Name the blood parasite species.
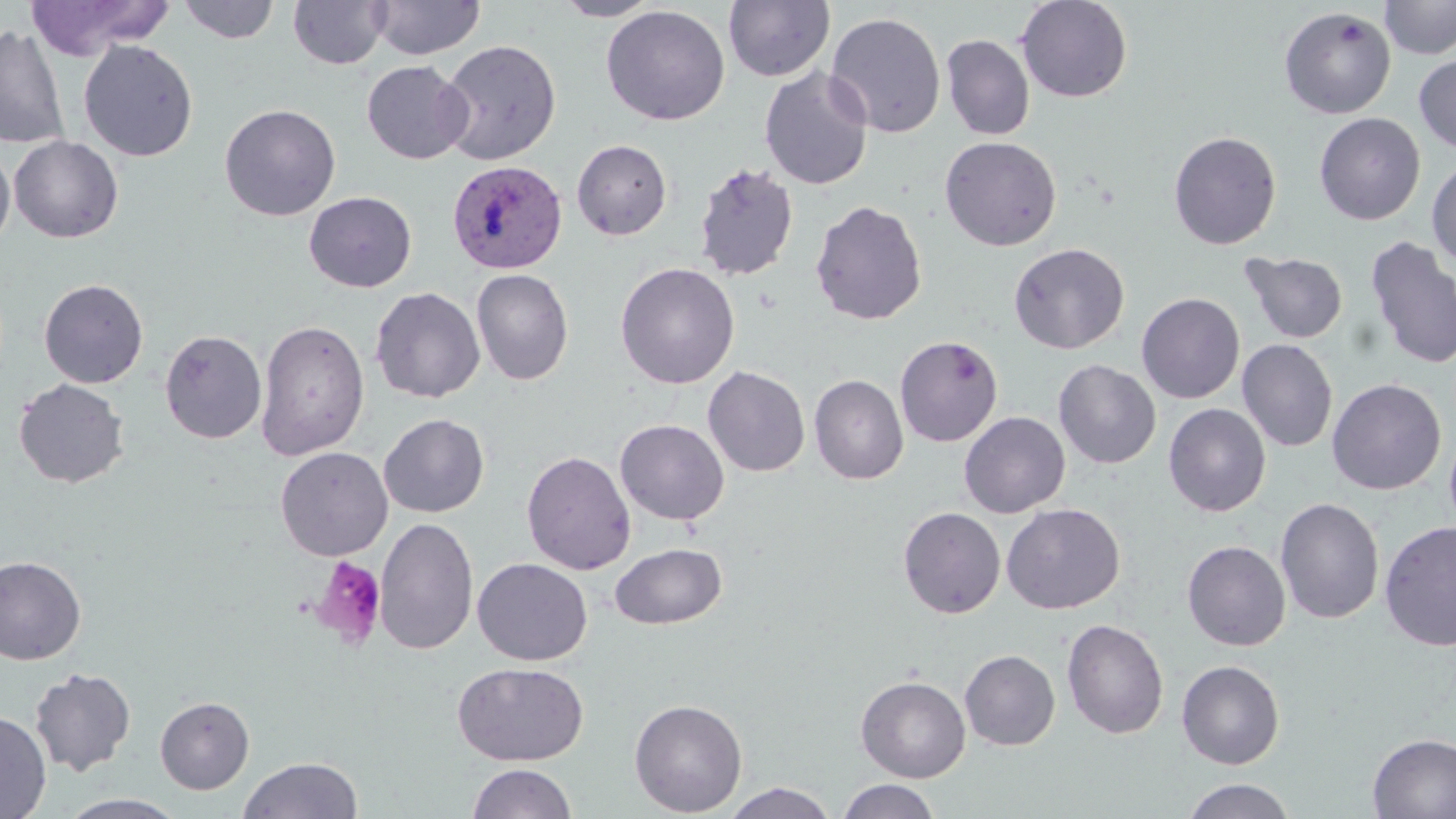
Plasmodium vivax.

{
  "platelet_locations": "approximate bounding boxes as (x1, y1, x2, y2) in pixels: (310, 555, 387, 649)",
  "plasmodium_vivax_infected_red_blood_cell_locations": "approximate bounding boxes as (x1, y1, x2, y2) in pixels: (447, 159, 567, 274)",
  "modality": "optical microscopy",
  "field_of_view": "single",
  "uninfected_red_blood_cell_locations": "approximate bounding boxes as (x1, y1, x2, y2) in pixels: (23, 0, 169, 60), (287, 0, 391, 70), (369, 0, 485, 60), (551, 0, 664, 21), (1016, 0, 1133, 103), (1380, 0, 1456, 60), (178, 1, 279, 44), (723, 1, 835, 82), (601, 4, 730, 126), (1279, 6, 1396, 119), (825, 11, 947, 138), (0, 25, 69, 149), (941, 34, 1035, 141), (438, 39, 561, 165), (79, 40, 199, 161), (1414, 53, 1456, 155), (361, 60, 473, 165), (759, 67, 873, 191), (219, 103, 341, 221), (1314, 112, 1425, 225), (1168, 130, 1282, 250), (9, 136, 123, 243), (939, 136, 1062, 251), (571, 139, 672, 240), (0, 144, 15, 251), (1426, 158, 1456, 269), (694, 162, 799, 282), (304, 190, 417, 293), (809, 200, 928, 326), (1352, 235, 1452, 497), (1364, 235, 1456, 370), (1009, 242, 1129, 354), (1240, 251, 1348, 344), (615, 262, 740, 389), (471, 268, 574, 385), (39, 278, 148, 388), (370, 286, 485, 403), (1136, 293, 1245, 404), (256, 319, 370, 460), (160, 330, 267, 444), (895, 334, 1003, 447), (1237, 338, 1338, 452), (1053, 359, 1161, 469), (703, 366, 810, 477), (809, 374, 909, 484), (13, 378, 129, 488), (1327, 378, 1446, 495), (1164, 403, 1271, 517), (959, 411, 1070, 518), (378, 413, 489, 518), (614, 419, 729, 526), (275, 446, 393, 561), (521, 450, 636, 575), (1275, 497, 1385, 624), (1001, 503, 1125, 614), (898, 506, 1006, 618), (375, 517, 479, 655), (1379, 520, 1456, 652), (1182, 541, 1291, 651), (609, 542, 727, 629), (0, 555, 86, 665), (472, 558, 592, 666), (1061, 619, 1169, 739), (960, 649, 1060, 750), (1176, 660, 1285, 769), (452, 661, 589, 766), (29, 667, 136, 776), (856, 675, 971, 782), (155, 696, 254, 794), (629, 698, 748, 816), (0, 711, 51, 818), (1367, 733, 1456, 818), (238, 756, 363, 818), (466, 762, 577, 819), (1181, 778, 1296, 819), (837, 779, 941, 819), (722, 782, 838, 819), (58, 793, 188, 818)",
  "magnification": "1000x",
  "image_size": "1456×819 pixels",
  "preparation": "thin blood film",
  "stain": "May-Grünwald-Giemsa"
}